State the blood parasite species.
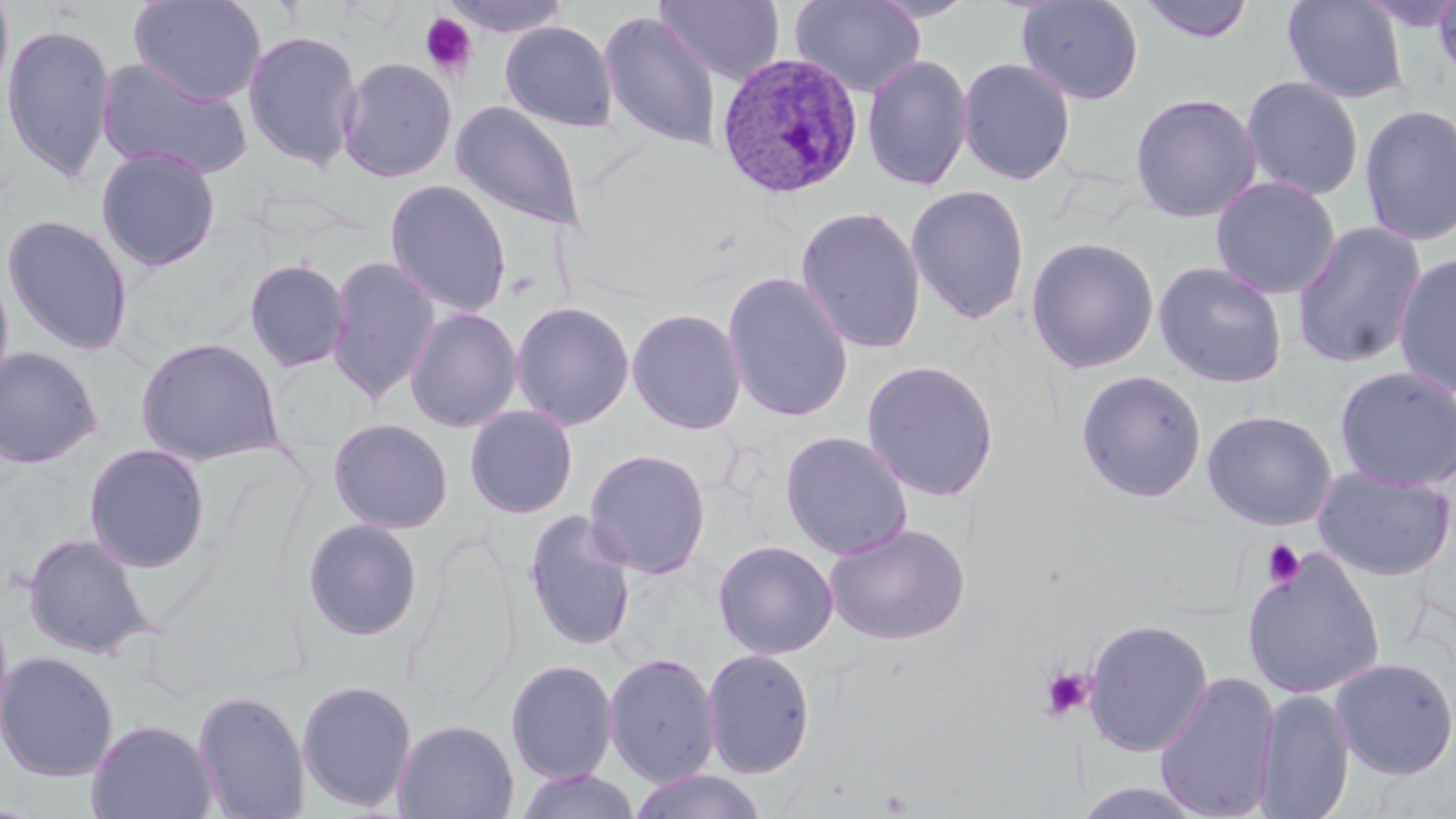
Plasmodium ovale.

uninfected red blood cell locations = approximate bounding boxes as named x1/y1/x2/y2 corners in pixels: (x1=0, y1=0, x2=14, y2=106), (x1=129, y1=0, x2=267, y2=105), (x1=438, y1=0, x2=574, y2=38), (x1=654, y1=0, x2=785, y2=86), (x1=789, y1=0, x2=927, y2=98), (x1=1015, y1=0, x2=1145, y2=105), (x1=1138, y1=0, x2=1256, y2=44), (x1=1281, y1=0, x2=1409, y2=104), (x1=1429, y1=0, x2=1456, y2=87), (x1=598, y1=10, x2=723, y2=151), (x1=500, y1=21, x2=619, y2=132), (x1=1, y1=22, x2=117, y2=183), (x1=242, y1=29, x2=363, y2=171), (x1=861, y1=54, x2=974, y2=191), (x1=96, y1=57, x2=254, y2=181), (x1=337, y1=57, x2=457, y2=182), (x1=957, y1=57, x2=1075, y2=185), (x1=1240, y1=75, x2=1364, y2=201), (x1=1129, y1=92, x2=1262, y2=223), (x1=452, y1=101, x2=587, y2=232), (x1=1358, y1=104, x2=1456, y2=247), (x1=95, y1=146, x2=222, y2=272), (x1=1210, y1=176, x2=1341, y2=300), (x1=385, y1=179, x2=512, y2=318), (x1=905, y1=184, x2=1031, y2=326), (x1=795, y1=205, x2=927, y2=355), (x1=1, y1=214, x2=134, y2=356), (x1=1291, y1=220, x2=1428, y2=369), (x1=1025, y1=236, x2=1160, y2=374), (x1=1393, y1=251, x2=1456, y2=398), (x1=326, y1=255, x2=441, y2=405), (x1=244, y1=258, x2=352, y2=372), (x1=1153, y1=260, x2=1289, y2=388), (x1=0, y1=262, x2=15, y2=399), (x1=721, y1=270, x2=854, y2=423), (x1=510, y1=301, x2=635, y2=431), (x1=405, y1=306, x2=523, y2=433), (x1=626, y1=307, x2=747, y2=435), (x1=134, y1=335, x2=284, y2=466), (x1=0, y1=347, x2=103, y2=468), (x1=860, y1=359, x2=1000, y2=502), (x1=1333, y1=366, x2=1455, y2=491), (x1=1075, y1=369, x2=1208, y2=503), (x1=464, y1=405, x2=579, y2=519), (x1=1202, y1=409, x2=1338, y2=530), (x1=328, y1=417, x2=454, y2=534), (x1=780, y1=430, x2=913, y2=560), (x1=83, y1=443, x2=212, y2=573), (x1=584, y1=448, x2=711, y2=579), (x1=1312, y1=465, x2=1456, y2=581), (x1=523, y1=508, x2=639, y2=651), (x1=302, y1=518, x2=424, y2=641), (x1=824, y1=522, x2=971, y2=646), (x1=23, y1=533, x2=154, y2=659), (x1=712, y1=539, x2=839, y2=660), (x1=1241, y1=549, x2=1385, y2=700), (x1=0, y1=600, x2=14, y2=742), (x1=1083, y1=617, x2=1213, y2=757), (x1=702, y1=647, x2=816, y2=779), (x1=0, y1=650, x2=119, y2=782), (x1=603, y1=651, x2=721, y2=788), (x1=1329, y1=657, x2=1456, y2=779), (x1=505, y1=658, x2=619, y2=785), (x1=1154, y1=670, x2=1281, y2=819), (x1=295, y1=678, x2=417, y2=813), (x1=1253, y1=687, x2=1355, y2=819), (x1=192, y1=689, x2=310, y2=819), (x1=86, y1=717, x2=219, y2=819), (x1=392, y1=718, x2=519, y2=819), (x1=514, y1=769, x2=642, y2=819), (x1=627, y1=769, x2=770, y2=819), (x1=1070, y1=781, x2=1213, y2=819)
platelet locations = approximate bounding boxes as named x1/y1/x2/y2 corners in pixels: (x1=419, y1=12, x2=477, y2=79), (x1=1261, y1=539, x2=1306, y2=589), (x1=1038, y1=666, x2=1093, y2=722)
stain = May-Grünwald-Giemsa
modality = optical microscopy
field of view = single
Plasmodium ovale-infected red blood cell locations = approximate bounding boxes as named x1/y1/x2/y2 corners in pixels: (x1=714, y1=52, x2=861, y2=199)
image size = 1456×819 pixels
magnification = 1000x
preparation = thin blood smear